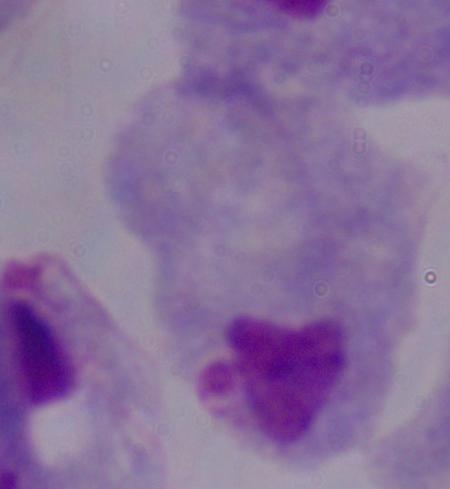

Summary:
  - Magnification: 1000x
  - Modality: photomicrograph
  - Identification: trichomonad